Assess this cell for malaria.
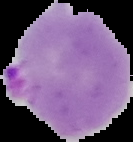
It is parasitized.

Image is 133×142 pixels. From a thin blood smear. Cell region segmented out of the field of view; the surrounding area is masked to black.